Name the parasite shown.
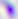

This is Toxoplasma gondii.

modality = micrograph
magnification = 400x